Describe the morphology of the red blood cells.
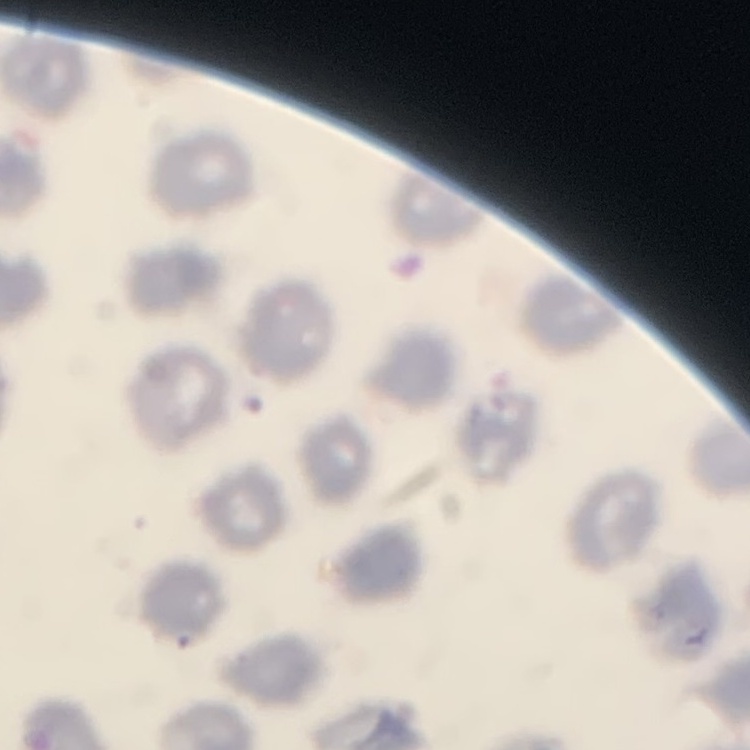

No rouleaux formation.

Summary:
  - Image type: one tile cut from a larger photomicrograph
  - Preparation: thin blood film
  - Stain: Field's or Giemsa